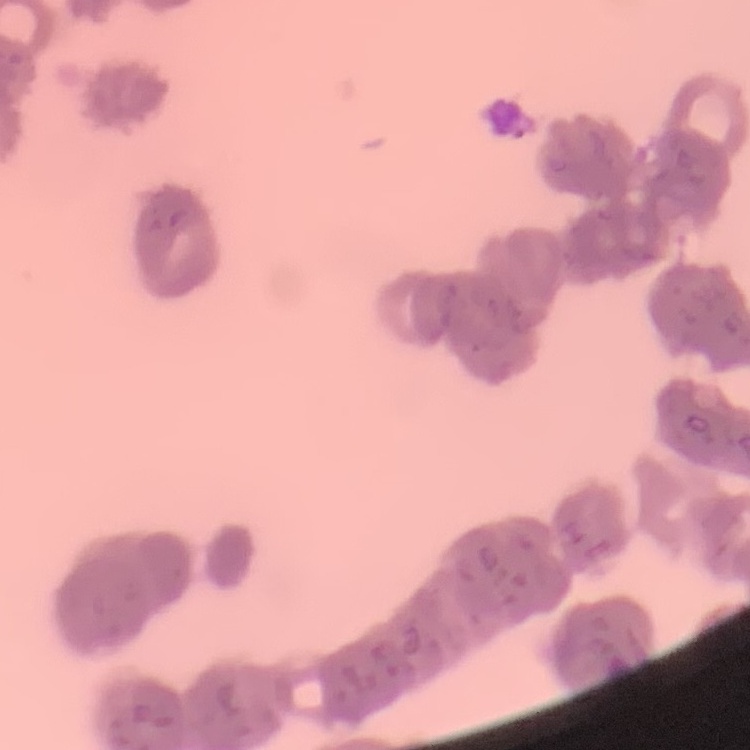
The erythrocytes exhibit rouleaux formation. Square crop of a larger photomicrograph. Stained with either Field's or Giemsa. Thin blood smear.